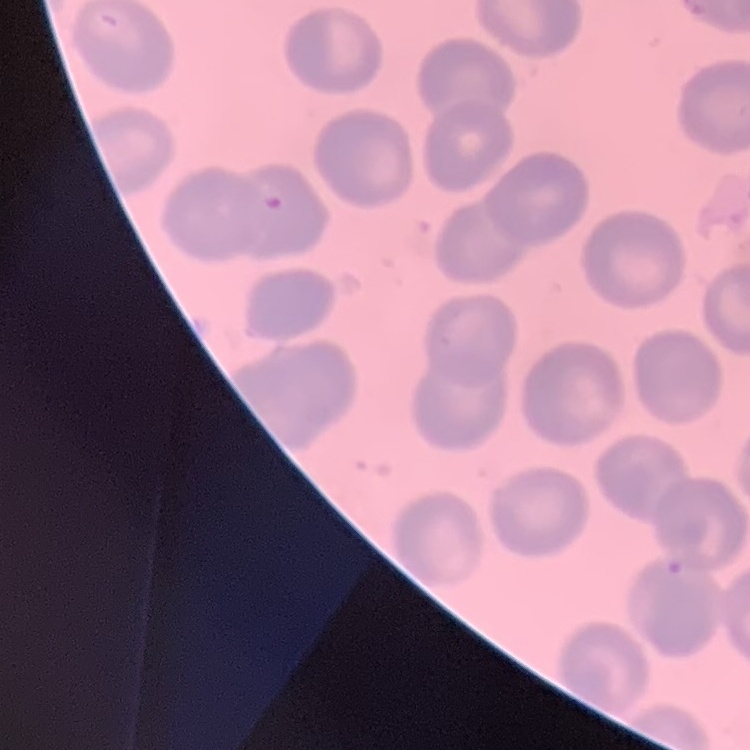 The red blood cells show no rouleaux formation. One tile cut from a larger photomicrograph. Thin blood smear. Field's or Giemsa stain.